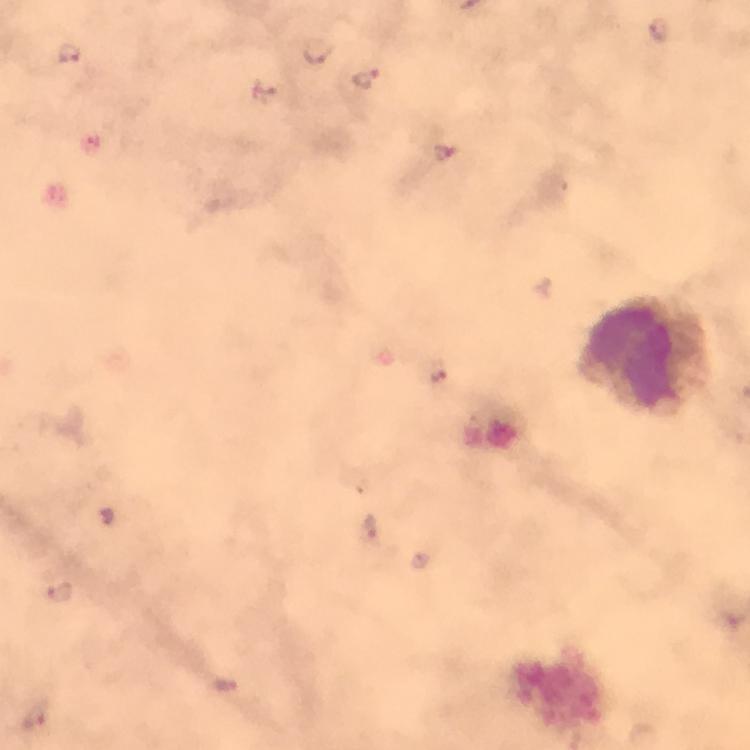

magnification: 100x
context: from a malaria diagnostic workup
image_size: 750×750 pixels
stain: Giemsa
cropped_from: one field of view
capture: smartphone mounted on the microscope
immersion_oil: applied
leukocyte_locations: 'approximate centers as (x, y) in pixels: (635, 356)'
preparation: thick blood smear
malaria_parasite_locations: 'approximate centers as (x, y) in pixels: (659, 30), (319, 50), (70, 54), (365, 79), (263, 90), (444, 152), (439, 377), (370, 530), (59, 591), (227, 685), (34, 715)'